Identify the preparation type.
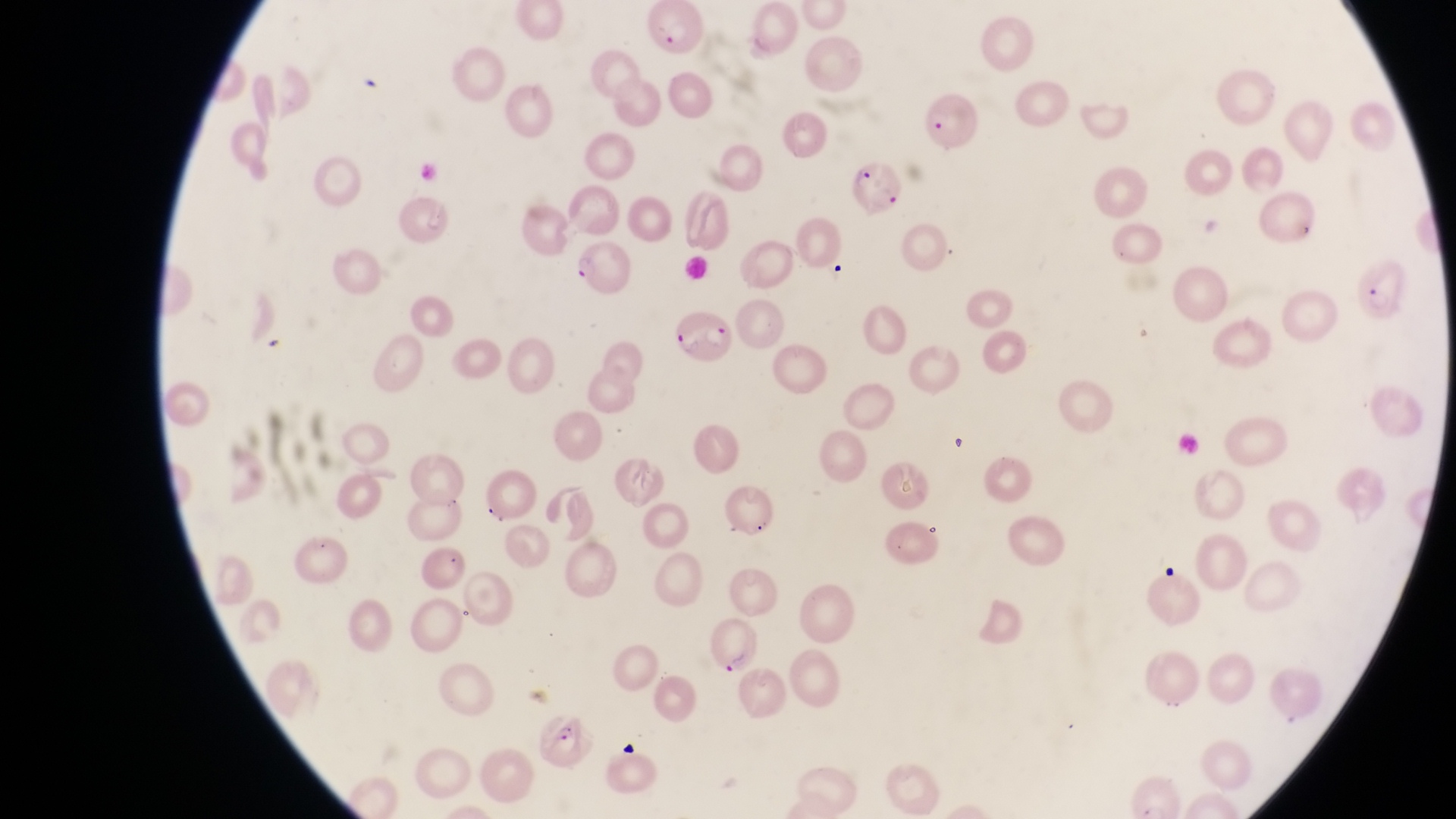
This is a thin smear.

Approximate bounding boxes as {left, top, right, bottom} in pixels. Parasitised red blood cell locations: {639, 2, 708, 54}, {922, 92, 981, 155}, {846, 162, 899, 217}, {570, 241, 629, 287}, {1357, 256, 1406, 316}, {670, 314, 739, 385}, {714, 620, 763, 678}, {538, 708, 590, 766}. Photographed through the eyepiece of an Olympus CX-23 microscope with a smartphone camera. At a magnification of 1000x. Sample from Uganda. Image is 1456×819 pixels. One field of view.